Name the parasite shown.
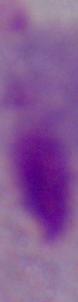
A trichomonad.

1000x magnification. Micrograph.